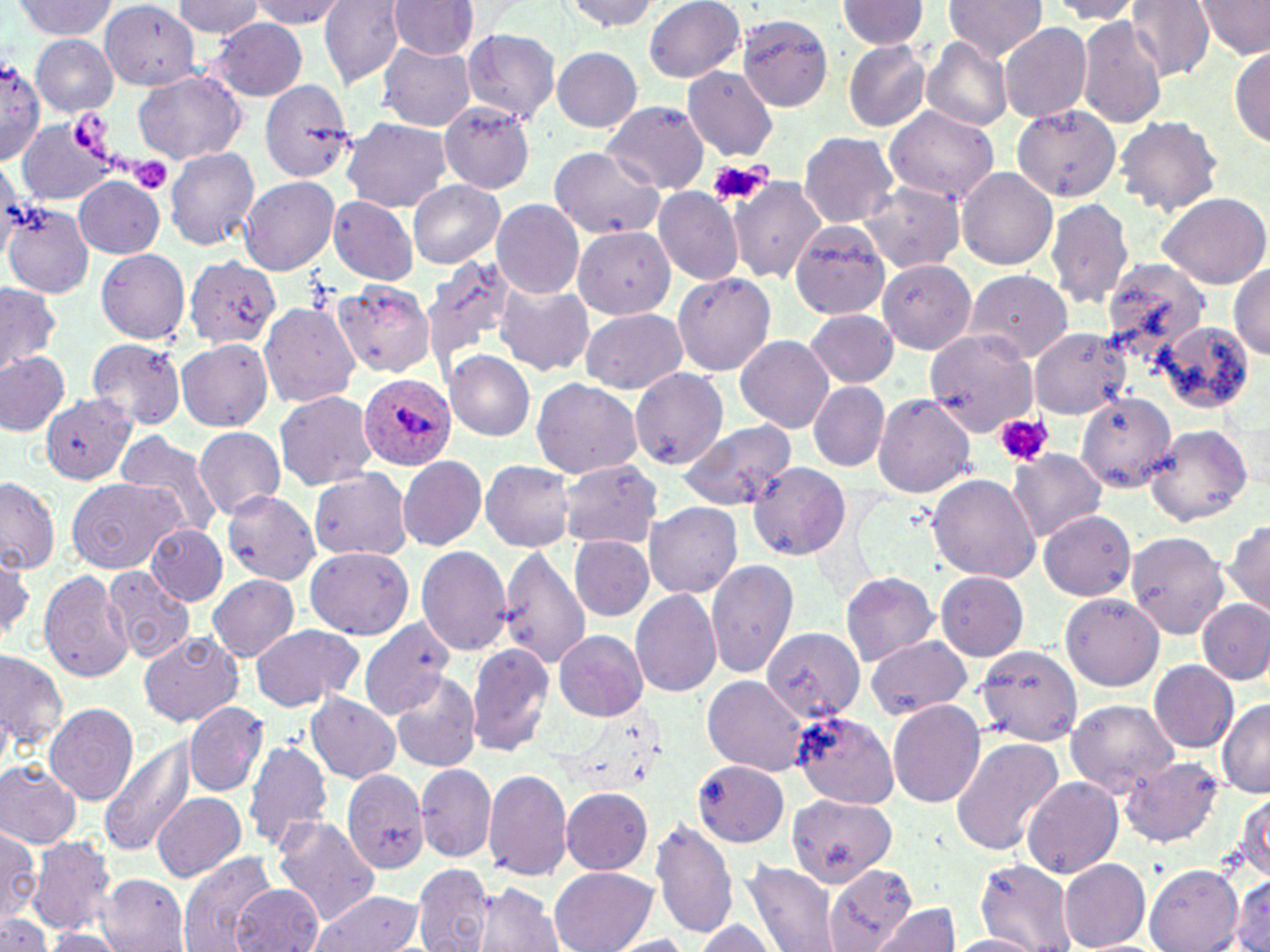

slide-level diagnosis = Plasmodium ovale
image size = 1270×952 pixels
stain = May-Grünwald-Giemsa
field of view = one of a larger specimen
uninfected red blood cell locations = approximate bounding boxes as (x1,y1)-(x2,y2) corner pairs in pixels: (173,0)-(260,38), (247,0)-(349,28), (319,0)-(406,87), (387,0)-(479,60), (644,0)-(746,83), (942,0)-(1048,60), (1196,0)-(1269,57), (560,1)-(663,32), (835,1)-(929,48), (1047,1)-(1145,22), (1126,1)-(1217,80), (12,2)-(119,40), (100,2)-(202,89), (735,15)-(833,113), (1075,15)-(1169,129), (208,17)-(310,102), (999,22)-(1092,122), (460,27)-(562,123), (29,34)-(117,115), (922,37)-(1013,131), (375,41)-(478,131), (842,41)-(931,132), (1230,43)-(1270,150), (551,45)-(642,131), (0,59)-(47,162), (683,66)-(778,161), (134,70)-(245,164), (260,82)-(359,185), (602,100)-(709,193), (439,101)-(537,194), (1013,105)-(1120,203), (883,107)-(999,203), (1114,115)-(1224,215), (341,117)-(451,212), (16,118)-(116,205), (798,131)-(899,228), (163,146)-(260,250), (548,146)-(665,239), (956,166)-(1058,270), (727,175)-(828,282), (72,176)-(165,259), (238,176)-(339,276), (408,180)-(504,267), (856,181)-(964,272), (652,187)-(744,284), (1157,191)-(1270,289), (327,196)-(418,285), (1045,196)-(1135,310), (490,198)-(584,300), (4,203)-(95,298), (787,219)-(891,318), (572,225)-(676,319), (95,247)-(190,344), (182,254)-(281,348), (418,254)-(520,373), (1097,257)-(1208,358), (877,259)-(976,355), (1231,261)-(1270,359), (963,269)-(1074,361), (671,270)-(775,375), (332,280)-(434,377), (492,281)-(594,376), (0,283)-(60,373), (259,300)-(359,409), (578,308)-(687,393), (802,308)-(900,390), (1158,321)-(1255,414), (1029,327)-(1132,420), (925,331)-(1037,436), (735,335)-(833,433), (86,338)-(187,429), (176,339)-(274,430), (0,349)-(72,436), (445,351)-(535,439), (628,367)-(729,469), (530,377)-(642,478), (808,381)-(890,471), (274,391)-(378,489), (1075,391)-(1177,494), (40,392)-(140,484), (871,393)-(978,498), (679,419)-(797,510), (1143,423)-(1256,526), (193,426)-(285,517), (115,432)-(224,536), (1009,449)-(1106,541), (398,455)-(485,551), (480,460)-(575,551), (559,460)-(665,548), (747,462)-(853,561), (308,467)-(413,561), (927,473)-(1041,584), (0,475)-(59,574), (68,476)-(185,574), (222,491)-(322,585), (645,501)-(742,598), (1037,510)-(1139,601), (1223,518)-(1270,618), (147,524)-(227,605), (1126,532)-(1230,637), (570,534)-(654,621), (416,545)-(513,654), (305,546)-(413,640), (499,546)-(592,669), (1,554)-(36,646), (705,557)-(799,678), (102,567)-(192,662), (38,569)-(134,683), (935,571)-(1029,660), (840,572)-(940,664), (208,575)-(299,661), (630,588)-(723,698), (1059,592)-(1165,691), (1196,598)-(1269,686), (357,618)-(456,719), (249,624)-(362,711), (761,628)-(866,722), (553,629)-(649,721), (138,631)-(242,727), (865,635)-(973,719), (464,643)-(555,756), (0,646)-(69,758), (975,646)-(1084,745), (1150,660)-(1240,752), (388,669)-(479,774), (702,675)-(809,775), (305,693)-(401,784), (888,699)-(986,808), (1065,699)-(1179,795), (1216,700)-(1270,798), (183,701)-(268,797), (44,702)-(137,805), (791,711)-(897,807), (99,736)-(198,857), (241,736)-(335,852), (949,736)-(1065,856), (1119,756)-(1224,848), (692,759)-(790,846), (0,760)-(84,850), (416,763)-(498,865), (342,767)-(430,875), (483,768)-(573,881), (1022,776)-(1121,880), (560,787)-(653,874), (1233,790)-(1268,881), (151,792)-(246,880), (787,793)-(896,888), (270,816)-(381,926), (651,818)-(738,939), (0,824)-(42,924), (26,836)-(119,934), (178,851)-(277,952), (1060,856)-(1151,950), (974,859)-(1079,950), (744,862)-(840,952), (823,863)-(918,951), (412,864)-(496,952), (1146,865)-(1244,950), (550,866)-(657,952), (1229,872)-(1270,952), (97,873)-(188,951), (235,882)-(322,952), (474,884)-(563,952), (308,889)-(423,952), (871,904)-(960,951), (0,913)-(53,952), (688,920)-(781,952), (41,928)-(128,951), (946,933)-(1045,952), (608,934)-(697,951), (1073,939)-(1170,952)
magnification = 1000x
Plasmodium ovale-infected red blood cell locations = approximate bounding boxes as (x1,y1)-(x2,y2) corner pairs in pixels: (359,374)-(457,471)
modality = light microscopy
preparation = thin blood film
platelet locations = approximate bounding boxes as (x1,y1)-(x2,y2) corner pairs in pixels: (64,110)-(112,159), (129,157)-(173,194), (708,160)-(772,206), (995,413)-(1054,466)